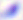
Summary:
  - Identification: Toxoplasma gondii
  - Modality: micrograph
  - Magnification: 400x